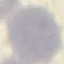

{
  "result": "no malaria parasites seen",
  "image_type": "cell patch, automatically extracted from a larger field of view and resized to 64 × 64 pixels",
  "preparation": "thin blood smear",
  "stain": "Giemsa",
  "capture": "smartphone through the microscope eyepiece"
}